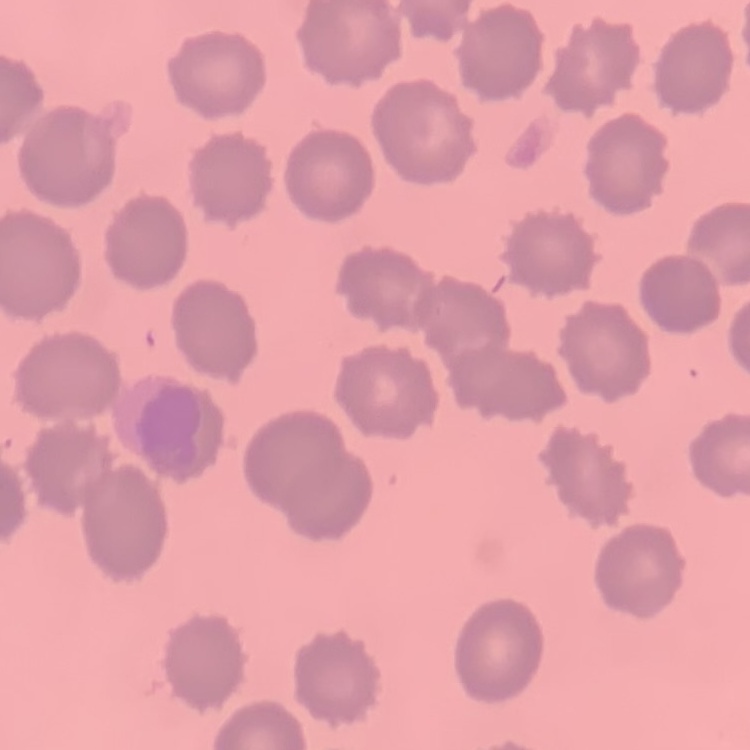

The red blood cells exhibit no rouleaux formation. Thin blood film. Field's or Giemsa stain. Square crop of a larger photomicrograph.